Assess this cell for malaria.
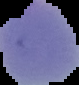
Uninfected.

Image is 79×85 pixels. From a thin blood smear. Cell region segmented out of the field of view; the surrounding area is masked to black.